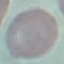
Result: no malaria parasites detected. Photographed with a smartphone camera at the microscope eyepiece. Thin blood smear. Cell patch, automatically extracted from a larger field of view and resized to 64 × 64 pixels. Giemsa stain.